Assess this cell for malaria.
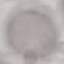
It is uninfected.

Summary:
  - Preparation: thin blood smear
  - Capture: smartphone through the microscope eyepiece
  - Image type: automatically extracted cell patch, resized to 64 × 64 pixels
  - Stain: Giemsa